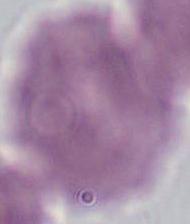

A red blood cell is seen. Captured at 1000x magnification. Photomicrograph.